Outline each blood parasite and name the species.
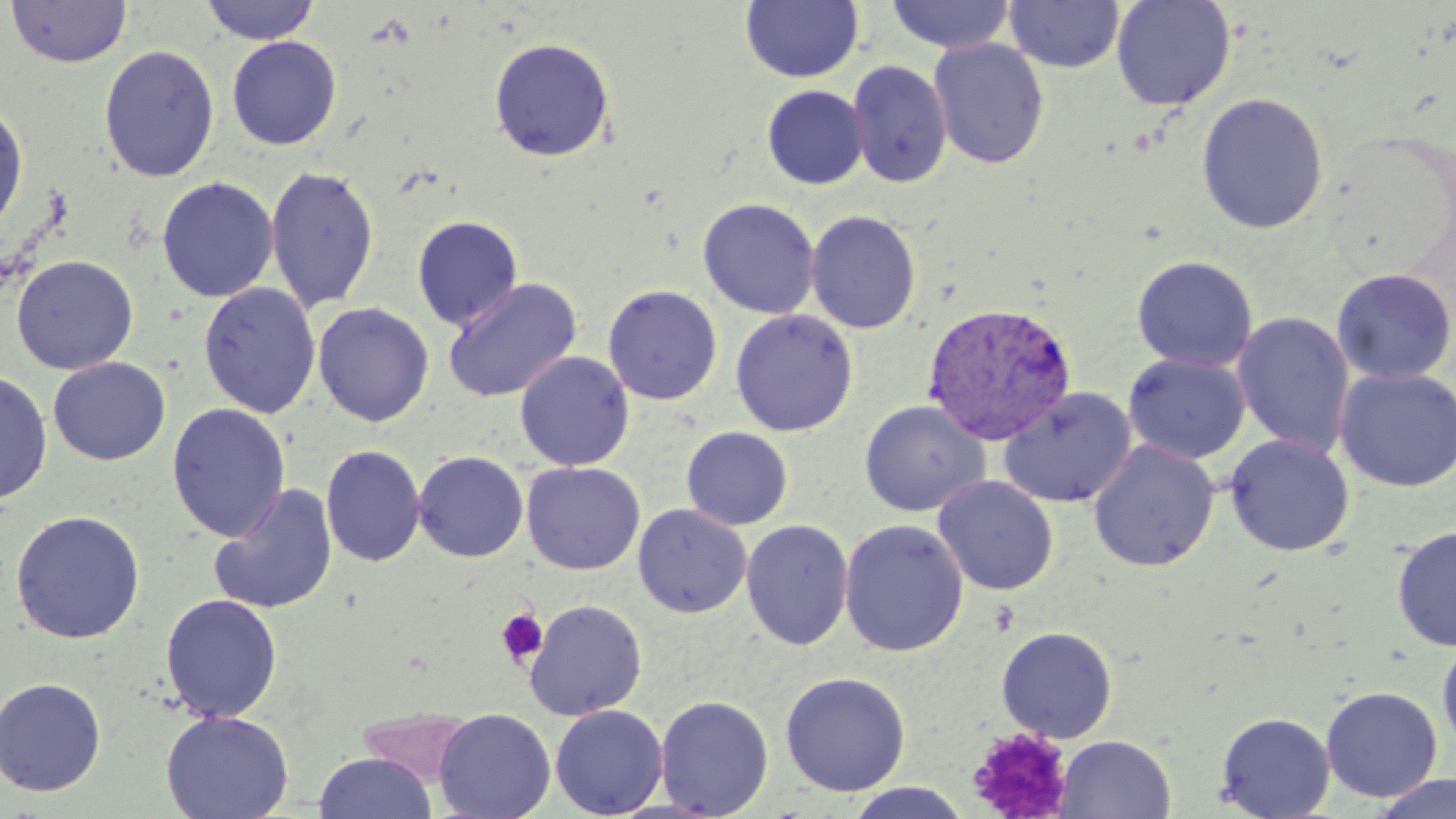
Approximate bounding boxes as named x1/y1/x2/y2 corners in pixels.
Plasmodium vivax-infected red blood cells: (x1=922, y1=301, x2=1077, y2=445).
No Plasmodium falciparum, Plasmodium ovale, Plasmodium malariae, Babesia divergens, or Trypanosoma brucei observed.

slide-level diagnosis = Plasmodium vivax
magnification = 1000x
platelet locations = approximate bounding boxes as named x1/y1/x2/y2 corners in pixels: (x1=496, y1=608, x2=548, y2=666), (x1=968, y1=727, x2=1074, y2=817)
uninfected red blood cell locations = approximate bounding boxes as named x1/y1/x2/y2 corners in pixels: (x1=5, y1=0, x2=131, y2=68), (x1=742, y1=0, x2=863, y2=83), (x1=886, y1=0, x2=1016, y2=54), (x1=1004, y1=0, x2=1124, y2=74), (x1=1110, y1=0, x2=1236, y2=111), (x1=200, y1=1, x2=320, y2=45), (x1=227, y1=36, x2=342, y2=150), (x1=488, y1=37, x2=615, y2=162), (x1=928, y1=38, x2=1050, y2=170), (x1=99, y1=45, x2=219, y2=182), (x1=847, y1=60, x2=951, y2=188), (x1=762, y1=85, x2=868, y2=189), (x1=1196, y1=92, x2=1329, y2=234), (x1=0, y1=100, x2=28, y2=237), (x1=265, y1=165, x2=380, y2=313), (x1=157, y1=177, x2=278, y2=302), (x1=698, y1=198, x2=820, y2=319), (x1=805, y1=210, x2=922, y2=335), (x1=412, y1=215, x2=523, y2=330), (x1=11, y1=255, x2=138, y2=374), (x1=1131, y1=256, x2=1258, y2=372), (x1=1331, y1=268, x2=1455, y2=384), (x1=442, y1=276, x2=582, y2=403), (x1=198, y1=282, x2=321, y2=418), (x1=603, y1=284, x2=723, y2=405), (x1=312, y1=302, x2=434, y2=428), (x1=730, y1=309, x2=858, y2=437), (x1=1231, y1=311, x2=1356, y2=457), (x1=515, y1=351, x2=634, y2=471), (x1=1124, y1=354, x2=1250, y2=464), (x1=48, y1=357, x2=170, y2=465), (x1=1334, y1=367, x2=1455, y2=492), (x1=0, y1=371, x2=53, y2=505), (x1=998, y1=387, x2=1136, y2=509), (x1=858, y1=400, x2=991, y2=517), (x1=167, y1=403, x2=291, y2=542), (x1=681, y1=426, x2=793, y2=530), (x1=1225, y1=434, x2=1355, y2=556), (x1=1087, y1=439, x2=1220, y2=571), (x1=321, y1=444, x2=425, y2=567), (x1=413, y1=451, x2=529, y2=562), (x1=522, y1=462, x2=645, y2=574), (x1=933, y1=475, x2=1059, y2=596), (x1=209, y1=483, x2=338, y2=615), (x1=632, y1=504, x2=751, y2=618), (x1=10, y1=510, x2=146, y2=644), (x1=741, y1=519, x2=854, y2=651), (x1=839, y1=519, x2=969, y2=657), (x1=1392, y1=526, x2=1456, y2=653), (x1=161, y1=593, x2=283, y2=723), (x1=524, y1=599, x2=648, y2=721), (x1=996, y1=626, x2=1118, y2=742), (x1=1437, y1=637, x2=1456, y2=754), (x1=780, y1=672, x2=911, y2=796), (x1=0, y1=677, x2=107, y2=796), (x1=1321, y1=685, x2=1442, y2=802), (x1=655, y1=695, x2=774, y2=818), (x1=550, y1=704, x2=668, y2=818), (x1=433, y1=708, x2=556, y2=819), (x1=355, y1=709, x2=479, y2=786), (x1=161, y1=710, x2=294, y2=819), (x1=1216, y1=711, x2=1335, y2=818), (x1=1056, y1=735, x2=1176, y2=818), (x1=314, y1=752, x2=436, y2=819), (x1=1370, y1=773, x2=1456, y2=818), (x1=843, y1=783, x2=972, y2=819)
stain = May-Grünwald-Giemsa
modality = optical microscopy
preparation = thin blood film
image size = 1456×819 pixels
field of view = single